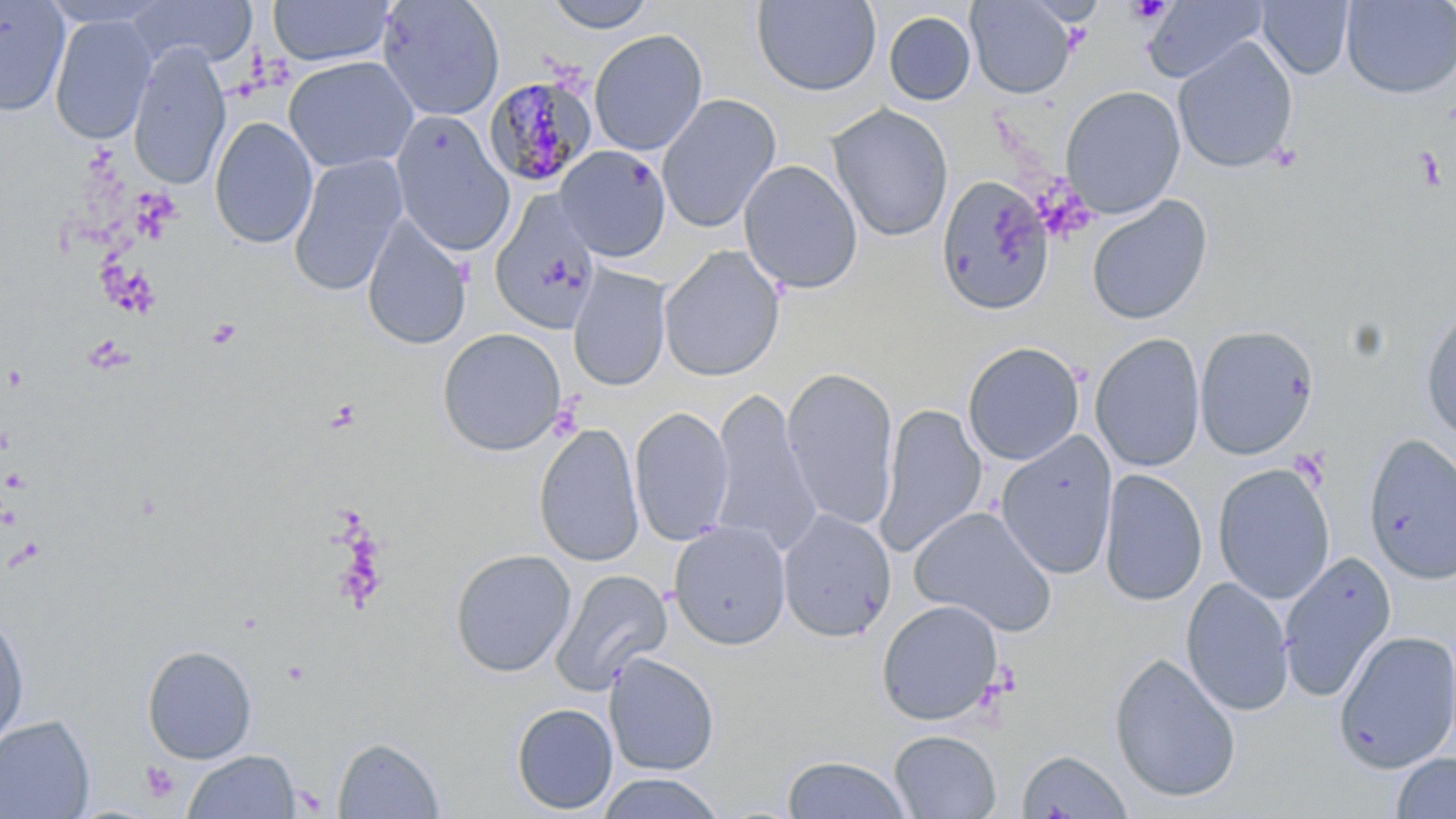

slide_level_diagnosis: Plasmodium malariae
modality: optical microscopy
image_size: 1456×819 pixels
uninfected_red_blood_cell_locations: 'approximate bounding boxes as [x1, y1, x2, y2] in pixels: [0, 0, 70, 116], [130, 0, 257, 68], [376, 0, 505, 122], [540, 0, 659, 33], [966, 0, 1076, 98], [1341, 0, 1456, 99], [268, 1, 396, 67], [751, 1, 882, 97], [1143, 1, 1269, 83], [1256, 1, 1354, 80], [883, 10, 977, 106], [49, 14, 157, 145], [589, 28, 708, 156], [1172, 37, 1298, 174], [127, 42, 231, 188], [283, 55, 418, 173], [1060, 85, 1185, 218], [657, 94, 781, 233], [827, 104, 954, 242], [390, 112, 514, 256], [209, 117, 318, 249], [555, 145, 672, 261], [287, 154, 408, 297], [738, 159, 862, 294], [935, 175, 1054, 316], [489, 191, 602, 335], [1085, 195, 1213, 325], [361, 214, 472, 351], [658, 245, 786, 382], [568, 266, 671, 391], [1420, 302, 1456, 444], [1194, 325, 1318, 459], [437, 327, 566, 455], [1090, 333, 1206, 473], [962, 341, 1085, 465], [781, 367, 900, 531], [708, 388, 821, 556], [877, 402, 986, 557], [629, 406, 734, 547], [533, 422, 644, 568], [995, 431, 1119, 581], [1363, 433, 1456, 584], [1212, 463, 1335, 604], [1099, 468, 1207, 607], [910, 506, 1057, 636], [778, 509, 896, 643], [668, 520, 792, 650], [450, 549, 576, 677], [1278, 551, 1396, 702], [550, 569, 672, 695], [1181, 576, 1294, 717], [876, 599, 1004, 726], [0, 607, 30, 750], [1333, 629, 1456, 774], [141, 644, 257, 764], [604, 652, 720, 776], [1109, 652, 1242, 804], [511, 702, 619, 815], [0, 714, 96, 819], [889, 730, 1001, 818], [333, 737, 445, 818], [1018, 748, 1133, 819], [183, 749, 300, 818], [1391, 752, 1456, 818], [781, 755, 911, 818], [595, 772, 725, 818]'
platelet_locations: 'approximate bounding boxes as [x1, y1, x2, y2] in pixels: [1412, 147, 1447, 191], [206, 318, 242, 349], [139, 760, 181, 805]'
magnification: 1000x
preparation: thin blood film
stain: May-Grünwald-Giemsa
field_of_view: one of a larger specimen
plasmodium_malariae_infected_red_blood_cell_locations: 'approximate bounding boxes as [x1, y1, x2, y2] in pixels: [484, 73, 598, 188]'